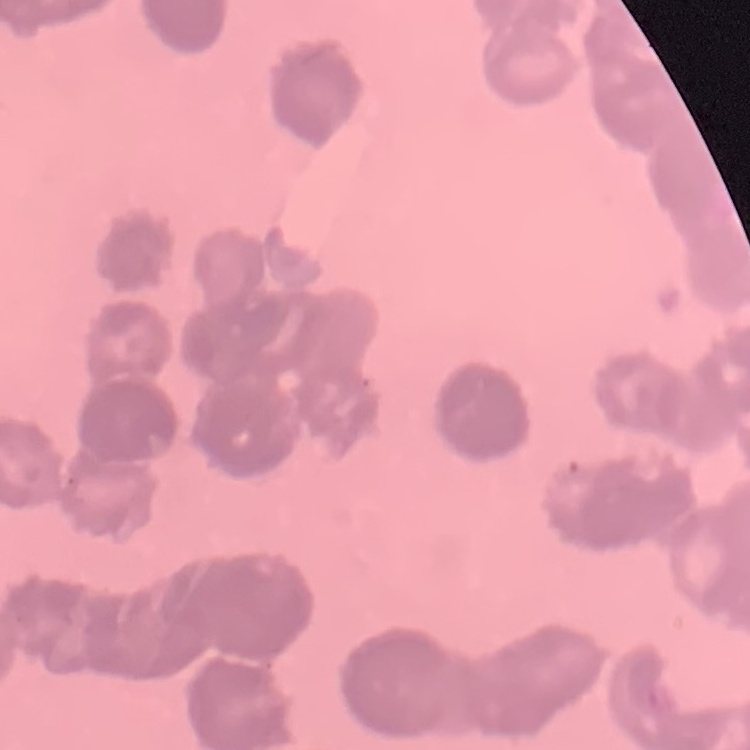
The erythrocytes show rouleaux formation. Thin peripheral smear. Square crop of a larger photomicrograph. Stained with either Field's or Giemsa.